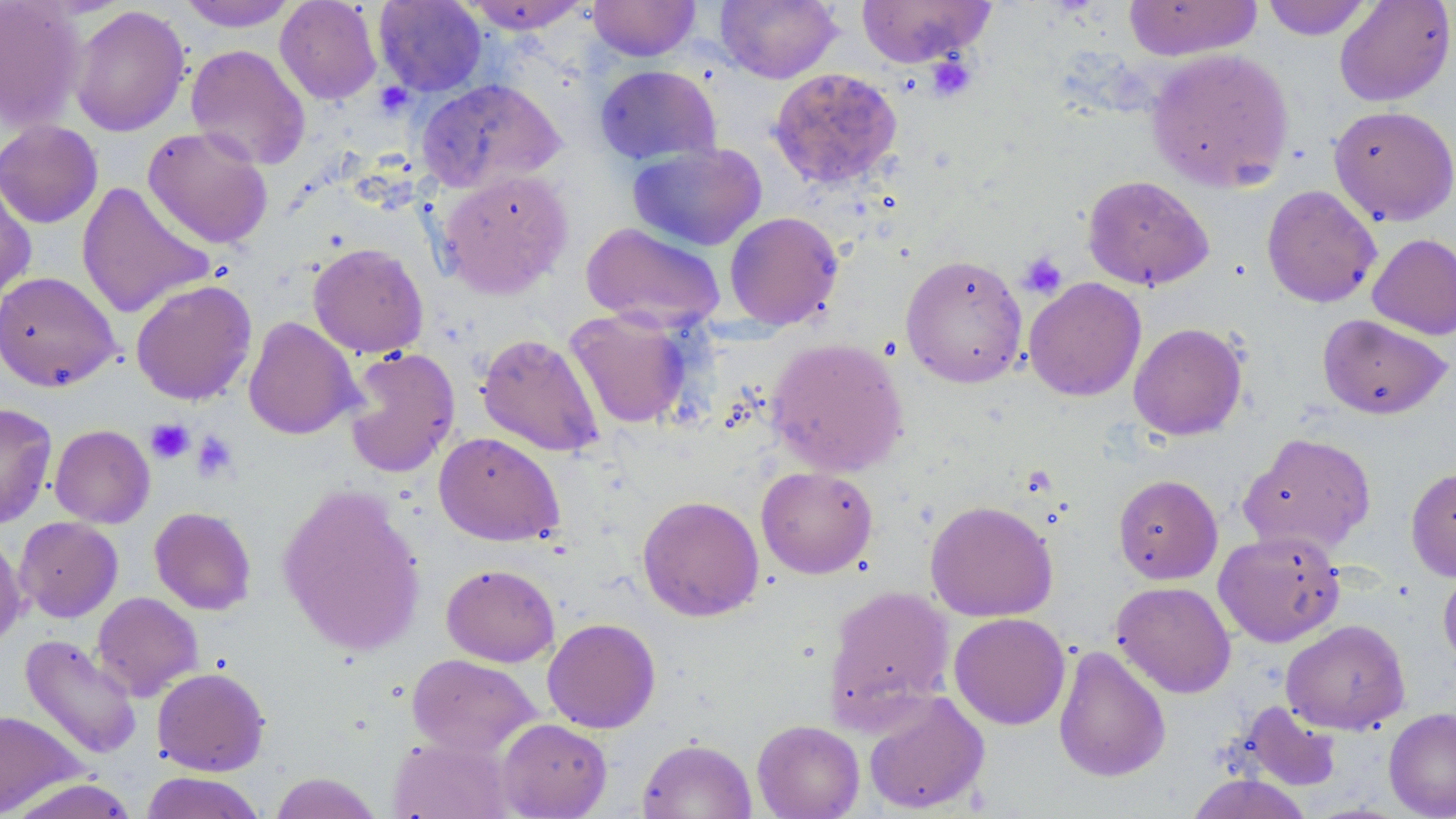
slide-level diagnosis = no evidence of blood parasites
image size = 1456×819 pixels
platelet locations = approximate bounding boxes as (x1, y1, x2, y2) in pixels: (925, 53, 979, 103), (1017, 252, 1067, 299), (147, 419, 194, 464), (190, 431, 239, 483)
uninfected red blood cell locations = approximate bounding boxes as (x1, y1, x2, y2) in pixels: (0, 0, 85, 131), (178, 0, 298, 31), (275, 0, 382, 105), (588, 0, 700, 61), (716, 0, 842, 84), (856, 0, 996, 68), (1122, 0, 1263, 61), (1259, 0, 1376, 40), (1334, 0, 1456, 107), (374, 1, 487, 96), (464, 1, 591, 33), (69, 5, 191, 136), (185, 44, 311, 171), (1146, 48, 1294, 192), (594, 65, 721, 165), (768, 67, 902, 190), (416, 78, 565, 193), (1328, 105, 1456, 226), (0, 120, 103, 228), (142, 126, 273, 250), (627, 142, 767, 251), (437, 170, 573, 299), (0, 173, 36, 306), (1082, 175, 1214, 291), (76, 181, 216, 319), (1261, 185, 1382, 308), (724, 210, 844, 330), (581, 222, 726, 330), (1368, 233, 1456, 340), (308, 242, 429, 358), (900, 253, 1028, 388), (0, 270, 121, 392), (1023, 277, 1146, 401), (130, 279, 257, 406), (564, 309, 693, 430), (1318, 314, 1452, 419), (243, 316, 361, 440), (1128, 322, 1248, 441), (476, 332, 604, 457), (765, 336, 908, 477), (343, 347, 460, 478), (1, 403, 57, 529), (50, 424, 155, 528), (434, 431, 564, 546), (1238, 432, 1377, 556), (756, 465, 878, 578), (1405, 465, 1456, 582), (1113, 474, 1223, 584), (277, 482, 427, 656), (637, 494, 764, 621), (925, 499, 1058, 622), (149, 506, 257, 615), (15, 517, 123, 622), (1213, 529, 1345, 647), (0, 530, 27, 650), (441, 563, 560, 667), (1438, 564, 1456, 671), (1111, 581, 1236, 698), (823, 585, 956, 724), (92, 591, 203, 701), (949, 612, 1070, 730), (542, 618, 661, 733), (1281, 619, 1410, 735), (19, 634, 142, 760), (1052, 644, 1171, 783), (406, 653, 541, 757), (152, 667, 270, 776), (863, 690, 990, 815), (1234, 700, 1343, 792), (1384, 707, 1456, 819), (0, 710, 85, 816), (496, 718, 612, 818), (752, 719, 865, 819), (388, 735, 511, 818), (637, 737, 757, 819), (140, 771, 267, 819), (269, 772, 384, 818), (1184, 774, 1315, 819), (5, 778, 141, 819)
stain = May-Grünwald-Giemsa
preparation = thin blood film
field of view = one of a larger specimen
magnification = 1000x
modality = optical microscopy